Describe the morphology of the erythrocytes.
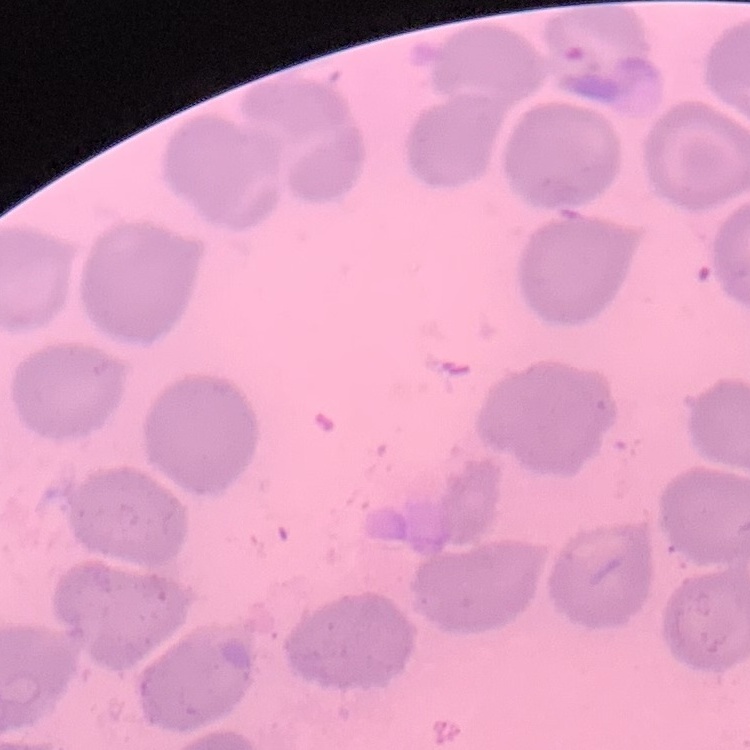
No rouleaux formation.

preparation = thin peripheral smear
stain = Field's or Giemsa
image type = one tile cut from a larger photomicrograph